Give the position of every malaria parasite.
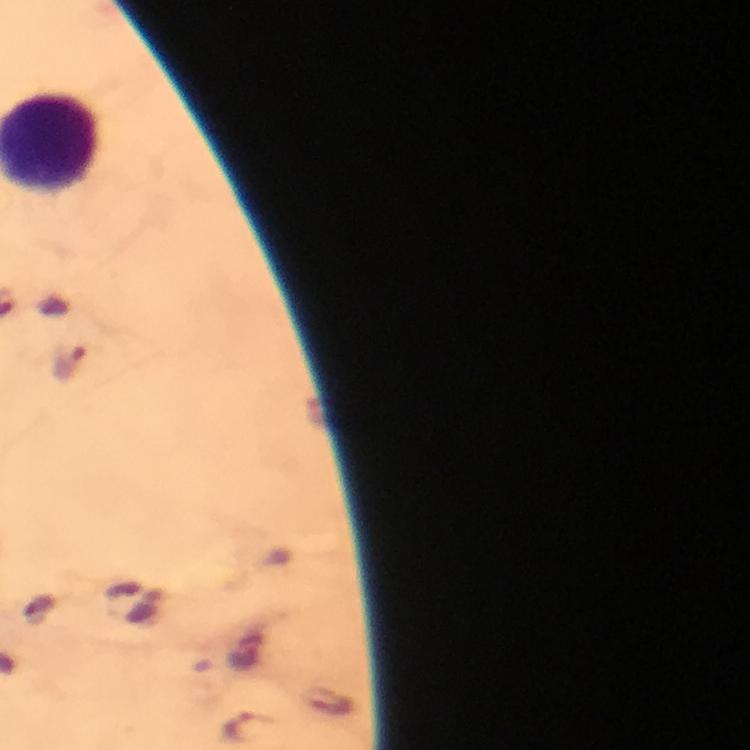
Approximate centers as [x, y] in pixels.
Malaria parasites: [70, 364], [245, 725].

context = from a diagnostic examination for malaria
image size = 750×750 pixels
cropped from = a single field of view
immersion oil = applied
capture = smartphone mounted on the microscope
preparation = thick smear
magnification = 100x
stain = Giemsa